State the preparation type.
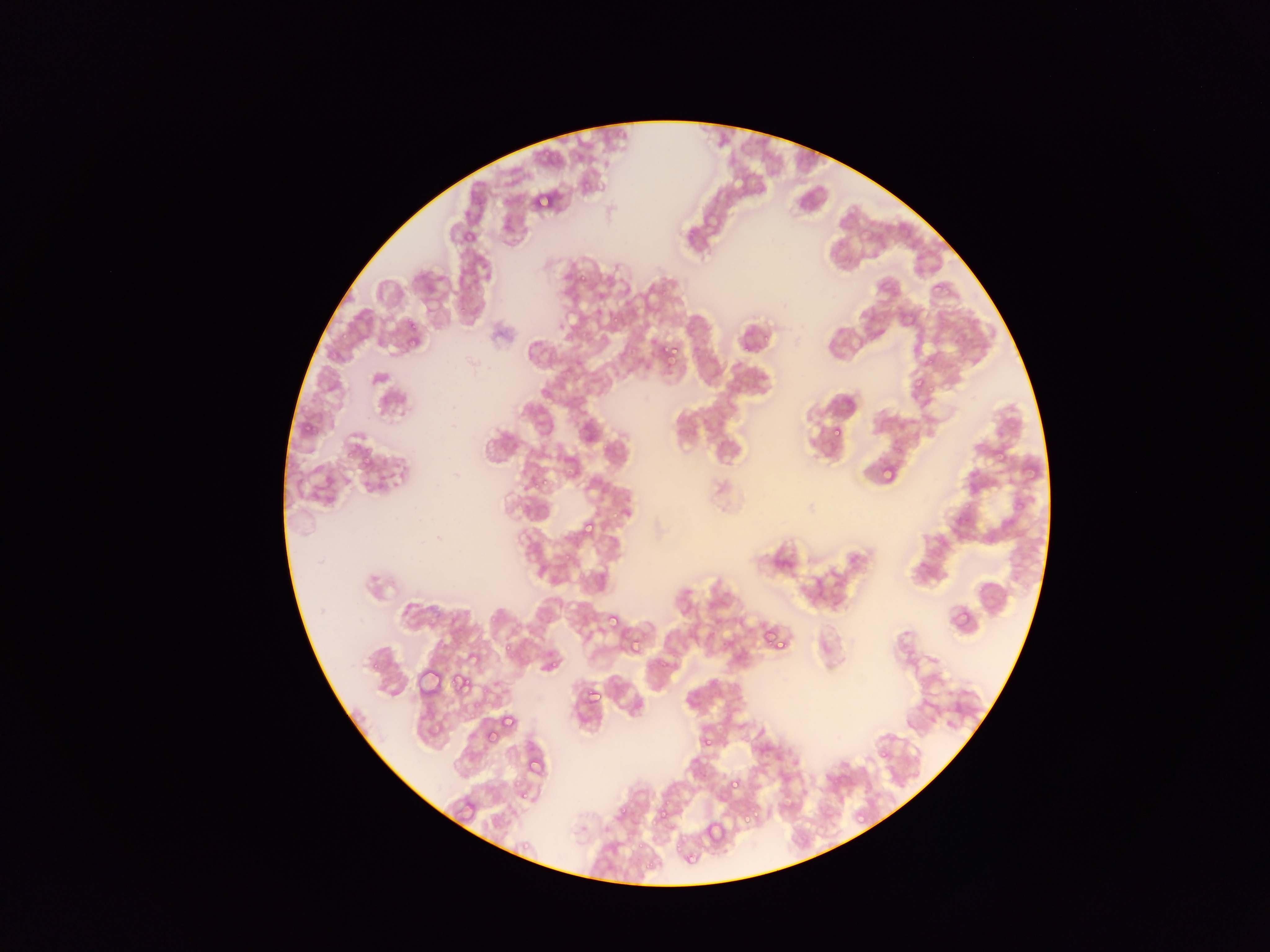
Thin blood film.

capture = mobile-phone photograph through a microscope
country = Ghana
field of view = single
Plasmodium parasite locations = approximate bounding boxes as {left, top, right, bottom} in pixels: {531, 189, 557, 211}, {930, 280, 947, 297}, {642, 282, 663, 306}, {405, 334, 421, 352}, {649, 337, 670, 359}, {657, 341, 680, 365}, {923, 351, 942, 372}, {910, 375, 927, 396}, {830, 428, 844, 439}, {995, 446, 1011, 462}, {1022, 460, 1040, 480}, {876, 462, 897, 484}, {579, 517, 600, 540}, {948, 604, 974, 633}, {603, 611, 623, 634}, {758, 622, 791, 655}, {626, 635, 645, 657}, {501, 638, 516, 656}, {416, 666, 447, 700}, {453, 673, 474, 697}, {581, 684, 603, 708}, {499, 712, 519, 734}, {483, 728, 499, 746}, {702, 736, 715, 746}, {726, 775, 745, 796}, {651, 804, 670, 827}, {703, 805, 738, 851}, {743, 809, 757, 823}, {854, 809, 869, 825}, {703, 819, 728, 847}
image size = 1270×952 pixels